Name the parasite shown.
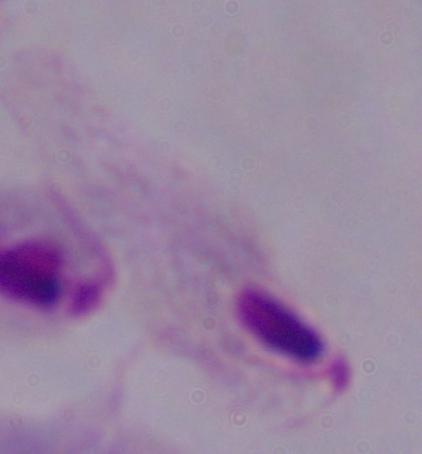

A trichomonad.

Summary:
  - Magnification: 1000x
  - Modality: photomicrograph